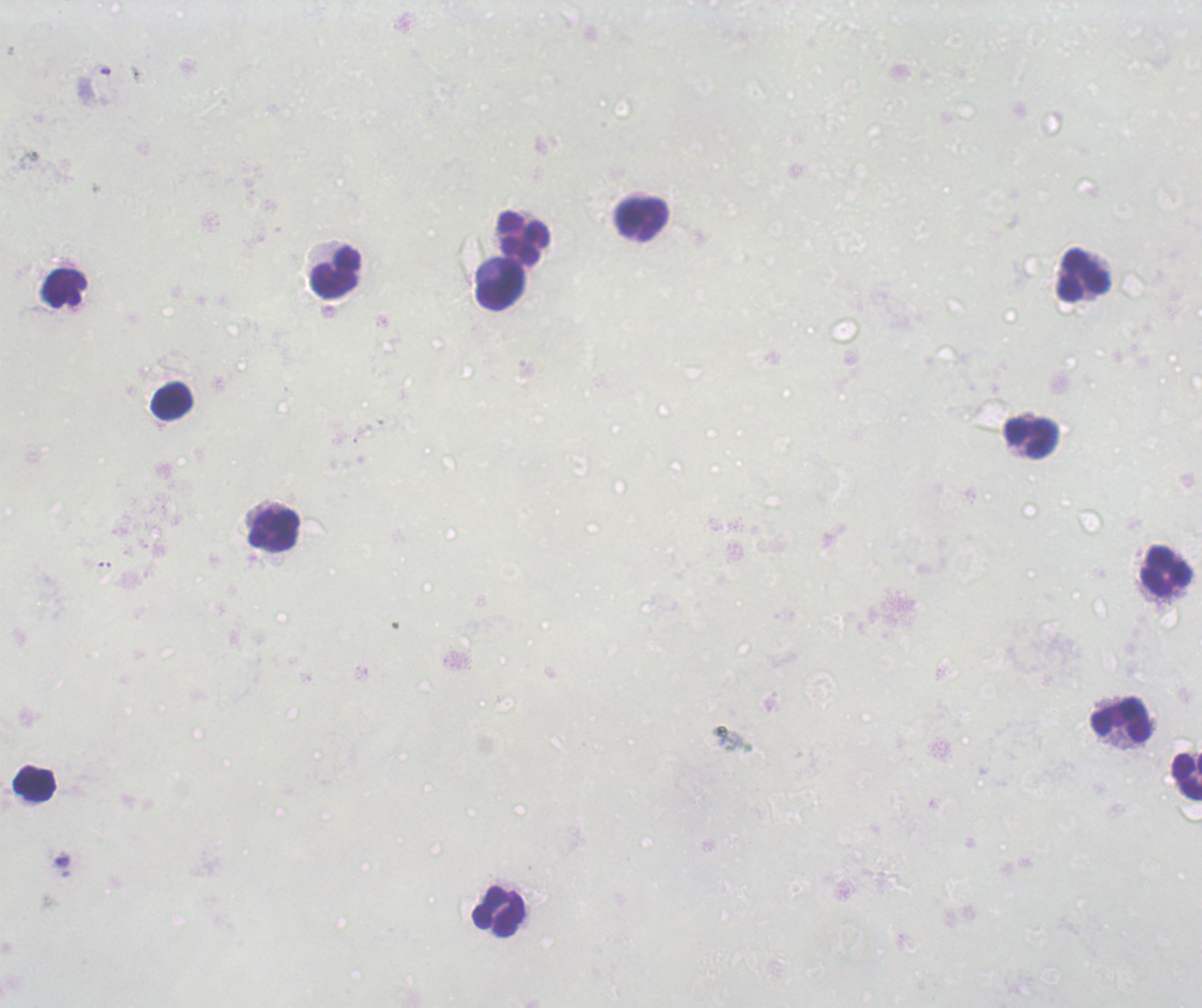
Approximate centers as [x, y] in pixels. Leukocyte locations: [641, 221], [525, 240], [336, 274], [1083, 276], [63, 287], [501, 287], [172, 400], [1031, 438], [275, 530], [1167, 571], [1120, 719], [1187, 777], [33, 784], [498, 912]. Captured at 100x magnification. Previously used in an actual diagnosis. Result: negative for malaria parasites. Single field of view. Thick blood smear. Image is 1202×1008 pixels. Background quality: unsatisfactory. Romanowsky stain.